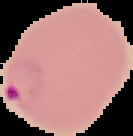
image_type: segmented cell region on a black background
image_size: 133×136 pixels
preparation: thin blood smear
malaria_status: parasitized